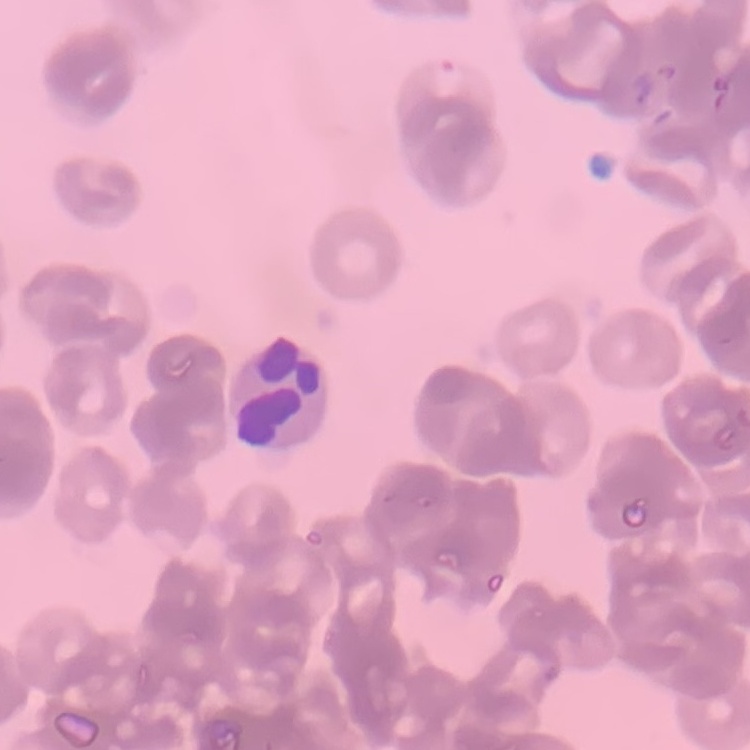
Summary:
  - Red blood cell morphology: rouleaux formation
  - Image type: square crop of a larger photomicrograph
  - Stain: Field's or Giemsa
  - Preparation: thin blood smear